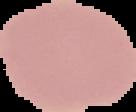

preparation = thin blood smear
image type = segmented cell region on a black background
image size = 136×112 pixels
malaria status = uninfected